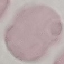
Summary:
  - Result: no malaria parasites detected
  - Preparation: thin blood film
  - Stain: Giemsa
  - Image type: automatically extracted cell patch, resized to 64 × 64 pixels
  - Capture: smartphone camera at the microscope eyepiece